State which cell type is depicted.
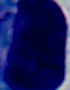

A leukocyte.

Summary:
  - Modality: photomicrograph
  - Magnification: 1000x